Assess the morphology of the erythrocytes.
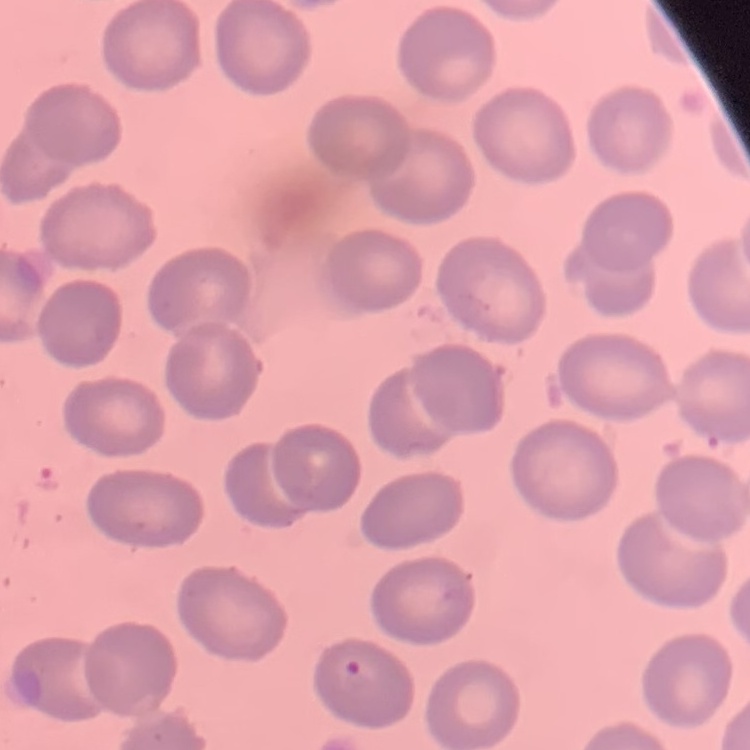
No rouleaux formation.

stain = Field's or Giemsa
preparation = thin peripheral smear
image type = square crop of a larger photomicrograph